Classify this cell by malaria status.
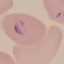

It is parasitized.

Summary:
  - Image type: cell patch, automatically extracted from a larger field of view and resized to 64 × 64 pixels
  - Capture: smartphone through the microscope eyepiece
  - Stain: Giemsa
  - Preparation: thin blood film